Name the parasite shown.
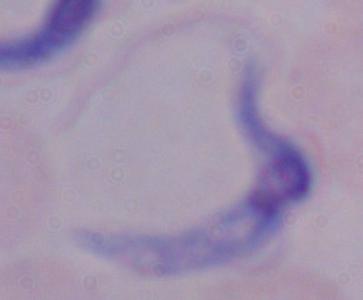
A trypanosome.

Summary:
  - Magnification: 1000x
  - Modality: photomicrograph